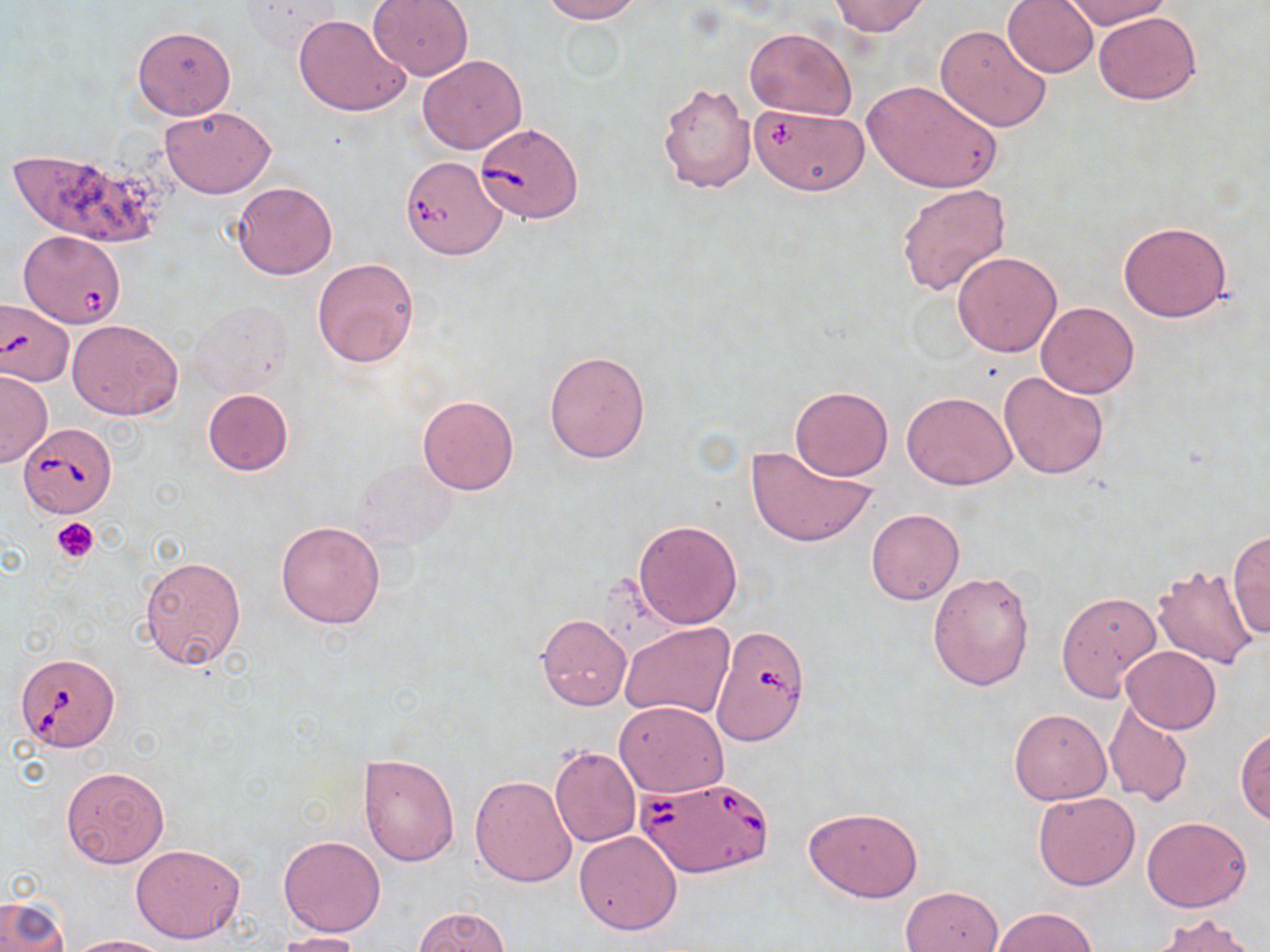
Babesia divergens-infected red blood cell locations = approximate bounding boxes as [x1, y1, x2, y2] in pixels: [475, 122, 582, 223], [400, 154, 508, 261], [18, 230, 127, 328], [0, 299, 73, 387], [20, 424, 117, 518], [712, 623, 814, 741], [15, 651, 118, 753], [639, 776, 771, 879]
slide-level diagnosis = Babesia divergens
magnification = 1000x
field of view = single
platelet locations = approximate bounding boxes as [x1, y1, x2, y2] in pixels: [51, 517, 100, 564]
modality = optical microscopy
uninfected red blood cell locations = approximate bounding boxes as [x1, y1, x2, y2] in pixels: [367, 0, 474, 80], [538, 0, 645, 23], [1002, 0, 1100, 78], [826, 1, 933, 36], [1060, 1, 1170, 30], [238, 2, 343, 55], [1093, 11, 1201, 105], [292, 13, 411, 117], [554, 21, 629, 81], [936, 24, 1052, 131], [132, 25, 237, 120], [744, 27, 857, 122], [417, 55, 526, 155], [863, 79, 1002, 193], [657, 82, 756, 194], [752, 104, 870, 196], [160, 106, 275, 199], [5, 147, 163, 250], [231, 182, 337, 280], [896, 182, 1011, 296], [1118, 221, 1232, 322], [952, 252, 1063, 357], [311, 257, 420, 368], [191, 300, 292, 398], [1037, 302, 1139, 398], [68, 319, 183, 420], [544, 349, 651, 464], [0, 370, 51, 467], [997, 371, 1109, 479], [790, 386, 893, 481], [203, 388, 294, 475], [903, 391, 1017, 489], [418, 395, 519, 496], [746, 443, 878, 548], [354, 459, 456, 551], [866, 508, 964, 605], [633, 519, 743, 629], [275, 520, 386, 629], [1230, 529, 1269, 639], [138, 554, 247, 671], [1152, 564, 1259, 669], [927, 570, 1035, 692], [1057, 591, 1163, 700], [534, 614, 632, 711], [620, 622, 733, 721], [1121, 646, 1221, 735], [1103, 699, 1194, 807], [615, 701, 729, 798], [1008, 708, 1111, 804], [1234, 727, 1270, 824], [549, 746, 641, 849], [357, 752, 459, 865], [61, 767, 170, 869], [470, 774, 578, 887], [1033, 792, 1140, 891], [804, 807, 924, 901], [1141, 815, 1253, 912], [575, 830, 683, 934], [278, 835, 385, 937], [131, 843, 246, 944], [901, 886, 1003, 952], [0, 893, 69, 952], [413, 905, 512, 952], [991, 907, 1098, 951], [1153, 914, 1258, 952], [277, 930, 364, 952], [67, 935, 171, 952]
preparation = thin blood smear
stain = May-Grünwald-Giemsa
image size = 1270×952 pixels